Give a bounding box for every malaria parasite.
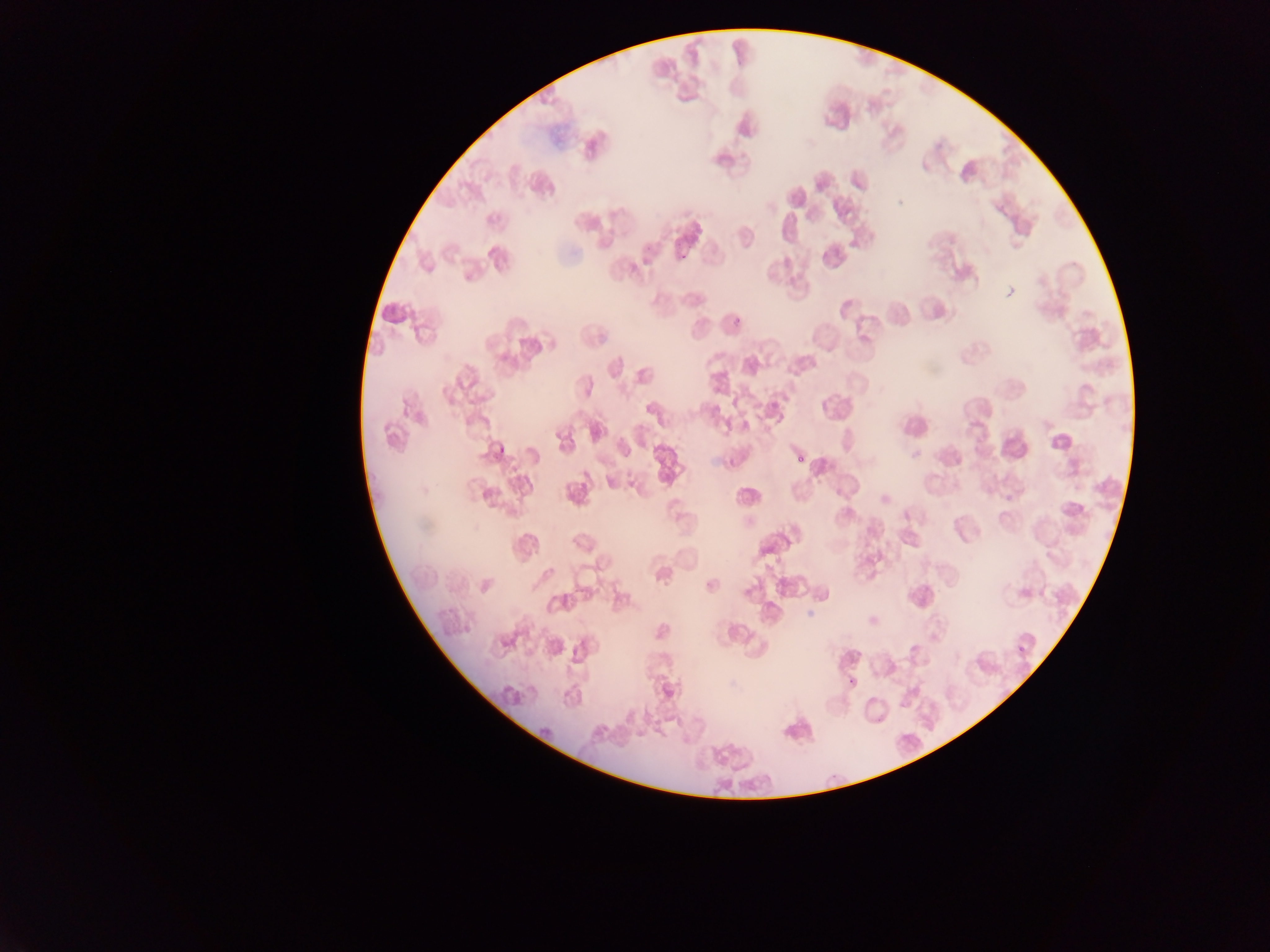

Approximate bounding boxes as left top right bottom in pixels.
Malaria parasites: 792 453 808 462; 1016 643 1028 653.

Collected in Ghana. Mobile-phone photograph taken through the microscope. Image is 1270×952 pixels. Thin blood film. One field of view.